Locate every malaria parasite.
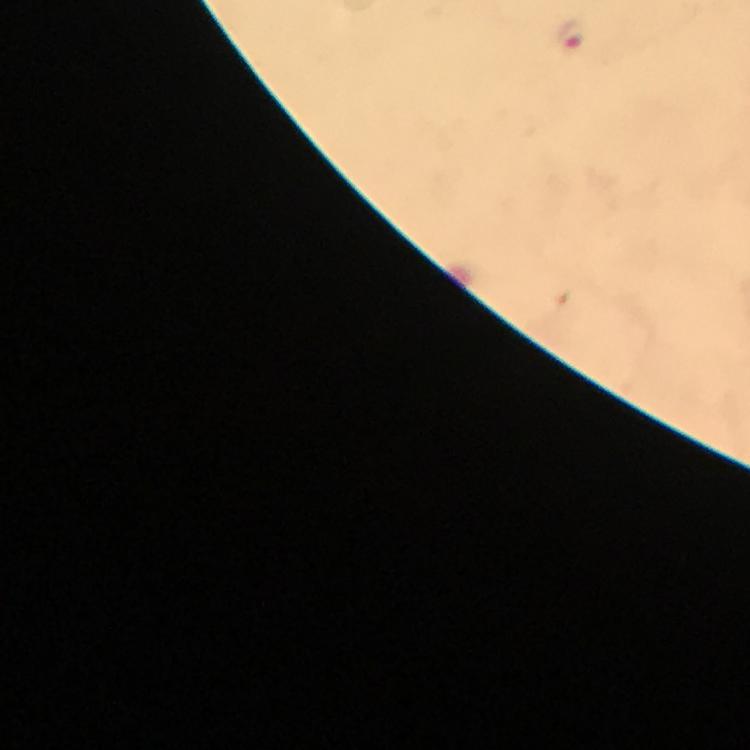
Approximate centers as (x, y) in pixels.
Malaria parasites: (571, 34).

Summary:
  - Capture: smartphone camera through the microscope
  - Magnification: 100x
  - Cropped from: a single field of view
  - Context: from a malaria diagnostic workup
  - Immersion oil: applied
  - Image size: 750×750 pixels
  - Stain: Giemsa
  - Preparation: thick blood smear